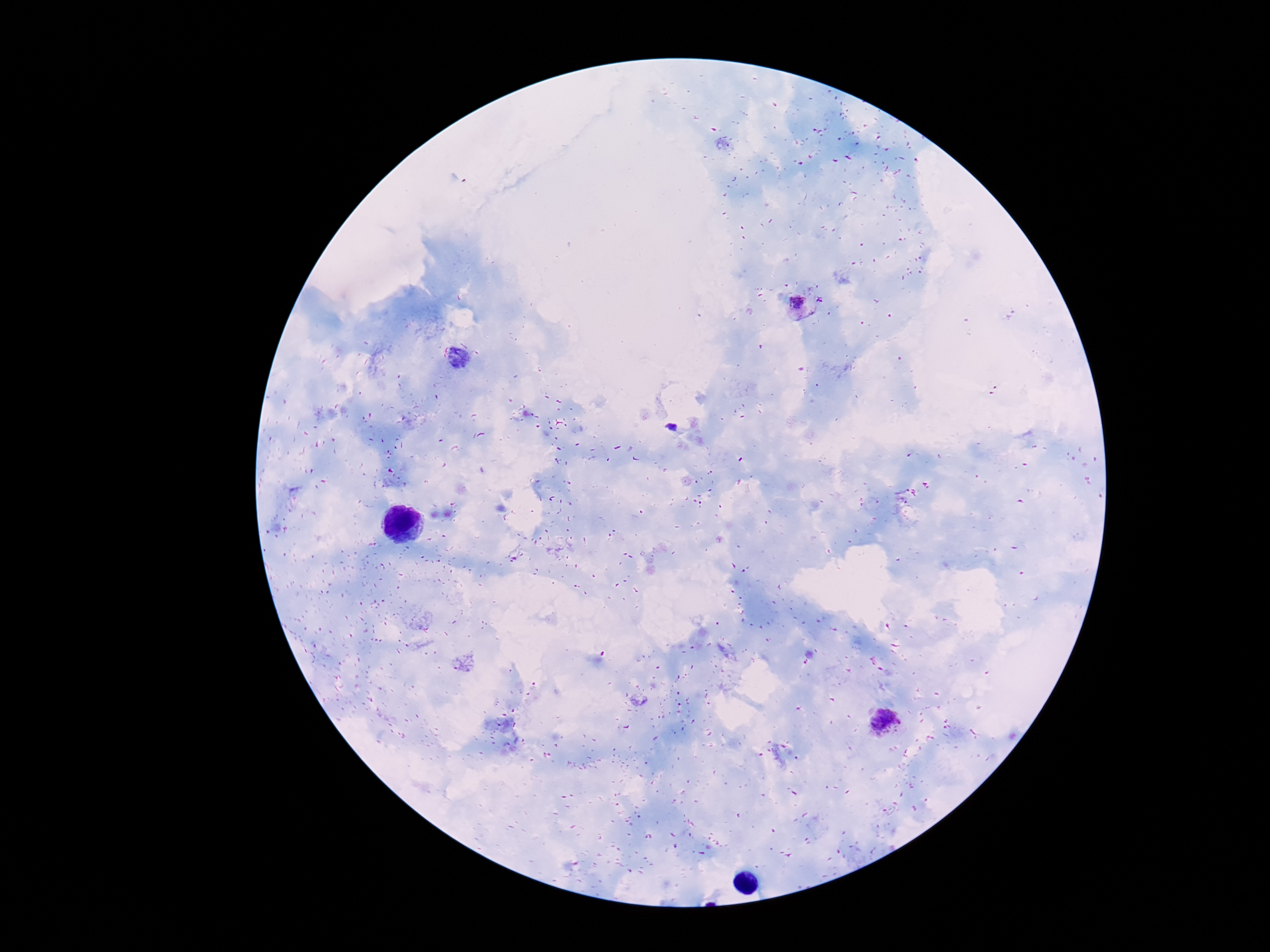
Approximate object centers, in pixels from the top-left corner.
Summary:
  - Plasmodium parasite locations: (x=798, y=304), (x=884, y=721)
  - Magnification: 100x
  - Field of view: one from this slide
  - Stain: Giemsa
  - Image size: 1270×952 pixels
  - Capture: smartphone camera through the microscope eyepiece
  - Patient malaria status: positive
  - Preparation: thick peripheral-blood smear